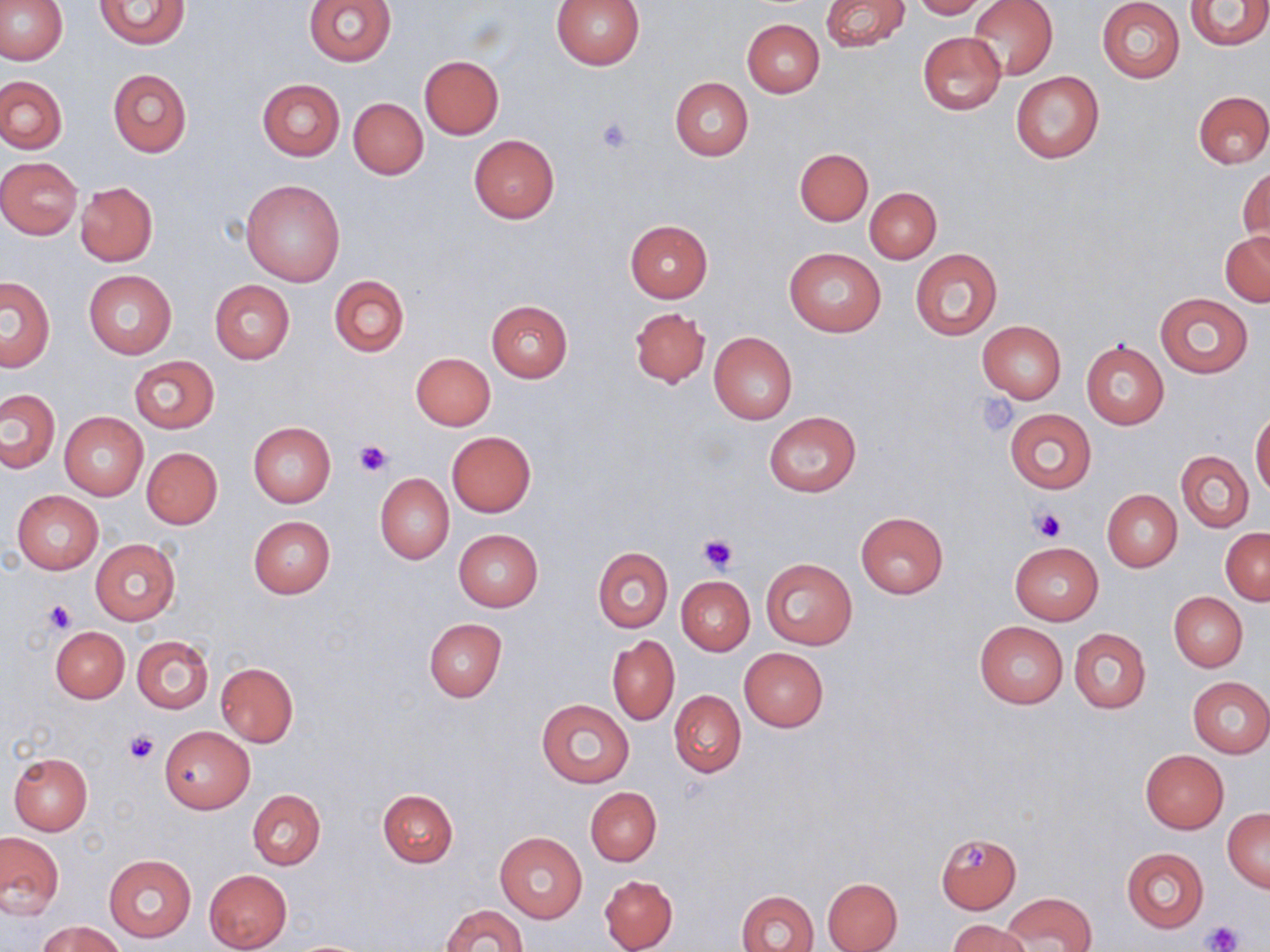 Approximate bounding boxes as named x1/y1/x2/y2 corners in pixels. Platelet locations: (x1=595, y1=116, x2=636, y2=155), (x1=974, y1=393, x2=1019, y2=437), (x1=354, y1=439, x2=393, y2=477), (x1=1032, y1=508, x2=1067, y2=542), (x1=699, y1=534, x2=736, y2=572), (x1=45, y1=600, x2=76, y2=632), (x1=124, y1=729, x2=159, y2=764), (x1=959, y1=845, x2=988, y2=871), (x1=1204, y1=921, x2=1241, y2=950). Uninfected red blood cell locations: (x1=0, y1=0, x2=67, y2=64), (x1=304, y1=0, x2=396, y2=67), (x1=820, y1=0, x2=909, y2=53), (x1=911, y1=0, x2=988, y2=19), (x1=967, y1=0, x2=1057, y2=80), (x1=1185, y1=0, x2=1270, y2=49), (x1=93, y1=1, x2=191, y2=49), (x1=551, y1=1, x2=645, y2=69), (x1=1097, y1=1, x2=1184, y2=83), (x1=741, y1=19, x2=824, y2=97), (x1=917, y1=31, x2=1007, y2=116), (x1=419, y1=55, x2=504, y2=138), (x1=107, y1=69, x2=190, y2=157), (x1=1011, y1=71, x2=1105, y2=163), (x1=0, y1=75, x2=66, y2=154), (x1=669, y1=77, x2=752, y2=161), (x1=256, y1=79, x2=344, y2=161), (x1=1194, y1=91, x2=1270, y2=169), (x1=348, y1=98, x2=428, y2=180), (x1=469, y1=135, x2=558, y2=223), (x1=795, y1=148, x2=872, y2=225), (x1=0, y1=156, x2=83, y2=238), (x1=1239, y1=165, x2=1269, y2=248), (x1=240, y1=178, x2=346, y2=287), (x1=75, y1=182, x2=157, y2=265), (x1=864, y1=187, x2=941, y2=263), (x1=624, y1=220, x2=713, y2=303), (x1=1221, y1=232, x2=1270, y2=306), (x1=783, y1=245, x2=886, y2=337), (x1=910, y1=247, x2=1002, y2=341), (x1=83, y1=269, x2=177, y2=358), (x1=329, y1=276, x2=409, y2=357), (x1=1, y1=278, x2=54, y2=371), (x1=209, y1=280, x2=294, y2=364), (x1=1156, y1=294, x2=1252, y2=377), (x1=485, y1=299, x2=573, y2=382), (x1=630, y1=307, x2=710, y2=388), (x1=977, y1=320, x2=1066, y2=403), (x1=709, y1=332, x2=797, y2=424), (x1=1081, y1=340, x2=1169, y2=429), (x1=410, y1=352, x2=496, y2=430), (x1=129, y1=355, x2=220, y2=434), (x1=0, y1=388, x2=59, y2=472), (x1=1004, y1=408, x2=1096, y2=494), (x1=1250, y1=409, x2=1270, y2=497), (x1=764, y1=411, x2=861, y2=498), (x1=59, y1=412, x2=148, y2=501), (x1=248, y1=422, x2=335, y2=507), (x1=447, y1=432, x2=536, y2=516), (x1=141, y1=447, x2=223, y2=529), (x1=1177, y1=450, x2=1253, y2=533), (x1=375, y1=473, x2=454, y2=563), (x1=12, y1=490, x2=104, y2=574), (x1=1102, y1=490, x2=1182, y2=571), (x1=856, y1=512, x2=948, y2=598), (x1=248, y1=516, x2=335, y2=598), (x1=454, y1=529, x2=543, y2=611), (x1=1221, y1=529, x2=1269, y2=605), (x1=91, y1=537, x2=181, y2=626), (x1=1010, y1=541, x2=1104, y2=625), (x1=593, y1=548, x2=672, y2=632), (x1=761, y1=558, x2=857, y2=648), (x1=677, y1=576, x2=755, y2=655), (x1=1170, y1=593, x2=1247, y2=670), (x1=422, y1=618, x2=507, y2=702), (x1=974, y1=621, x2=1068, y2=708), (x1=50, y1=625, x2=128, y2=702), (x1=1068, y1=628, x2=1150, y2=714), (x1=131, y1=635, x2=213, y2=714), (x1=607, y1=635, x2=679, y2=725), (x1=739, y1=647, x2=829, y2=732), (x1=216, y1=662, x2=298, y2=746), (x1=1187, y1=677, x2=1270, y2=758), (x1=669, y1=690, x2=746, y2=777), (x1=536, y1=697, x2=634, y2=787), (x1=160, y1=726, x2=254, y2=813), (x1=1140, y1=750, x2=1228, y2=833), (x1=9, y1=752, x2=93, y2=834), (x1=585, y1=787, x2=661, y2=865), (x1=248, y1=789, x2=326, y2=870), (x1=378, y1=789, x2=458, y2=869), (x1=1223, y1=809, x2=1270, y2=891), (x1=0, y1=831, x2=64, y2=919), (x1=495, y1=832, x2=587, y2=923), (x1=936, y1=833, x2=1022, y2=913), (x1=1121, y1=847, x2=1208, y2=934), (x1=103, y1=853, x2=196, y2=943), (x1=203, y1=869, x2=291, y2=950), (x1=599, y1=874, x2=678, y2=952), (x1=821, y1=877, x2=903, y2=952), (x1=737, y1=889, x2=819, y2=952), (x1=1004, y1=893, x2=1095, y2=952), (x1=440, y1=904, x2=528, y2=952), (x1=947, y1=919, x2=1032, y2=952), (x1=40, y1=921, x2=124, y2=952). Slide-level diagnosis: no evidence of blood parasites. Image is 1270×952 pixels. Optical microscopy. Single field of view. May-Grünwald-Giemsa stain. 1000x magnification. Thin blood film.